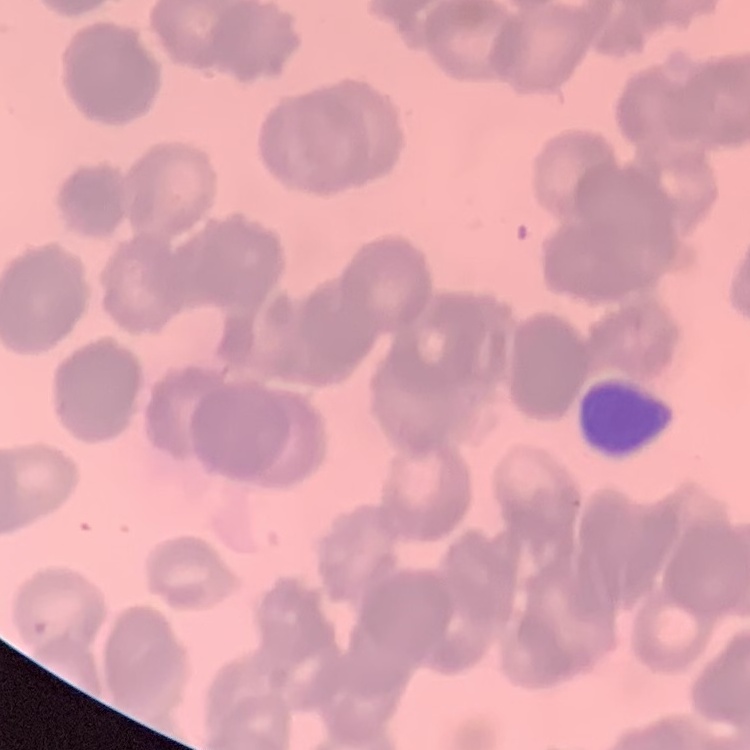

The erythrocytes exhibit rouleaux formation. Thin peripheral smear. Field's or Giemsa stain. Square crop of a larger photomicrograph.